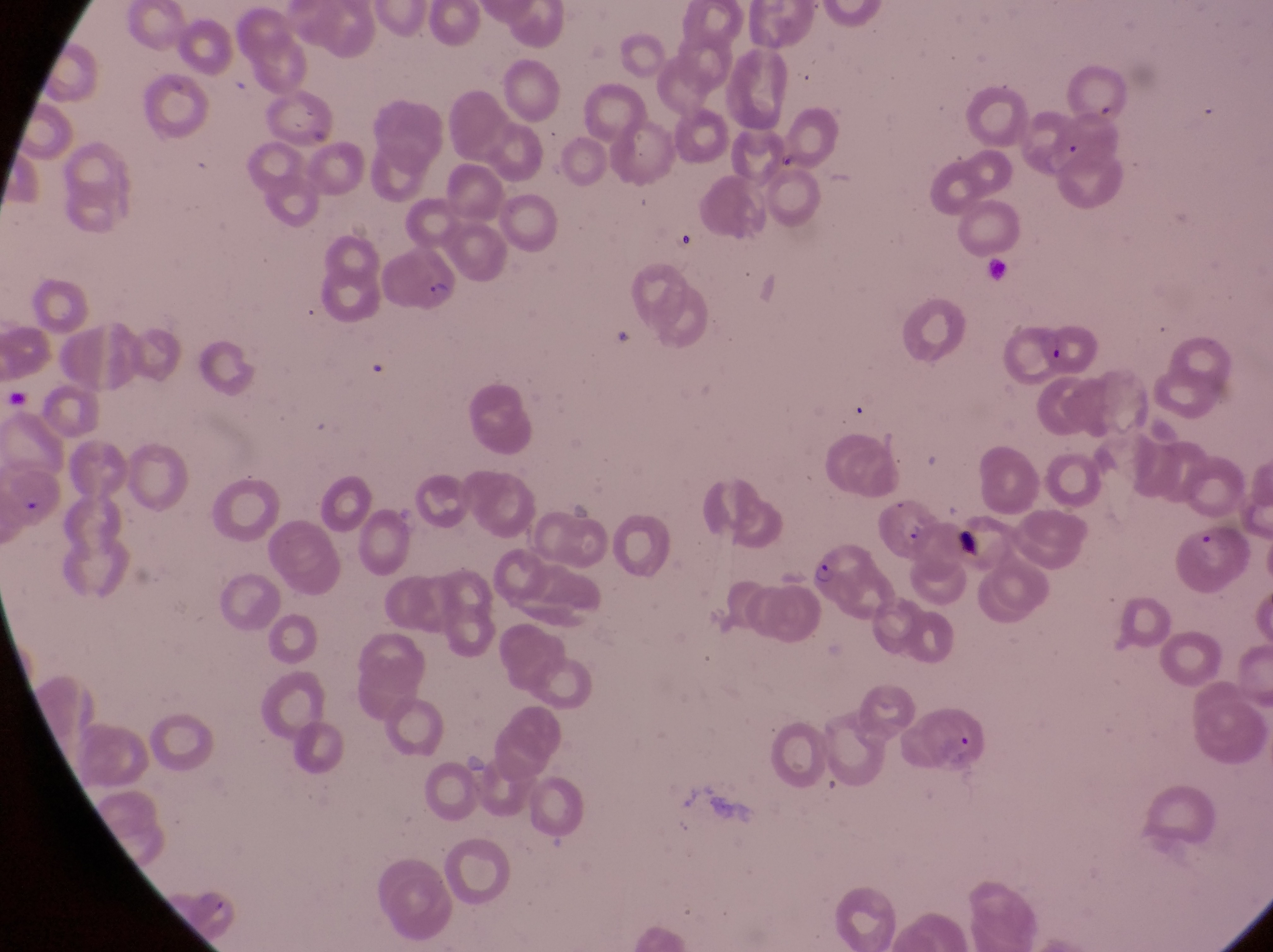
Approximate bounding boxes as [left, top, right, bottom] in pixels.
Summary:
  - Parasitised red blood cell locations: [375, 244, 462, 319], [1031, 313, 1105, 378], [879, 494, 942, 561], [803, 545, 895, 628], [909, 700, 992, 774]
  - Image size: 1273×952 pixels
  - Magnification: 1000x
  - Capture: smartphone photograph through the eyepiece of an Olympus CX-23 microscope
  - Preparation: thin blood film
  - Field of view: single
  - Country: Uganda